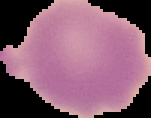
preparation: thin blood film
malaria_status: uninfected
image_type: cell region segmented out of the field of view; surrounding area masked to black
image_size: 151×118 pixels